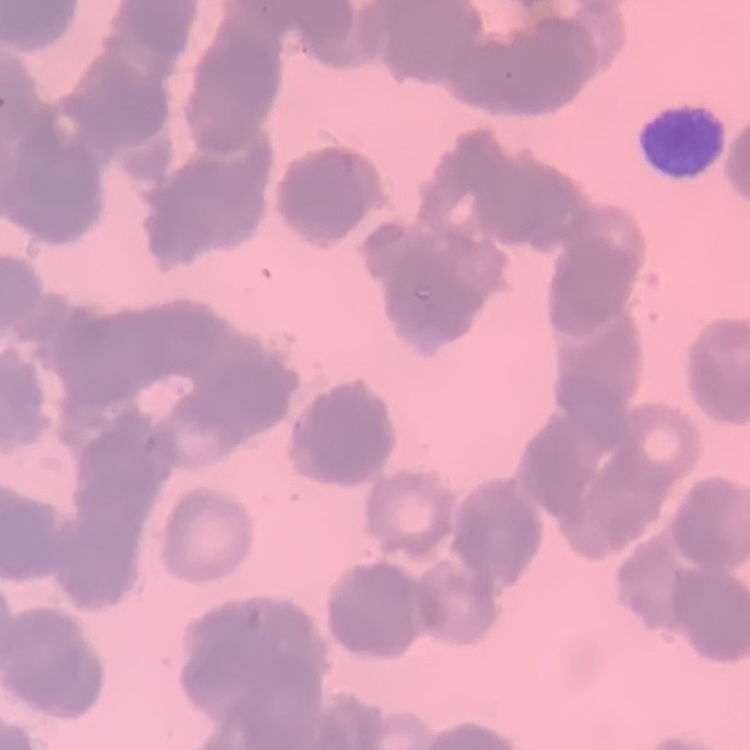

erythrocyte morphology = rouleaux formation
image type = one tile cut from a larger photomicrograph
preparation = thin peripheral smear
stain = Field's or Giemsa